State which cell type is depicted.
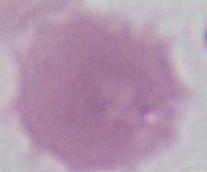

This is an erythrocyte.

Summary:
  - Magnification: 1000x
  - Modality: photomicrograph